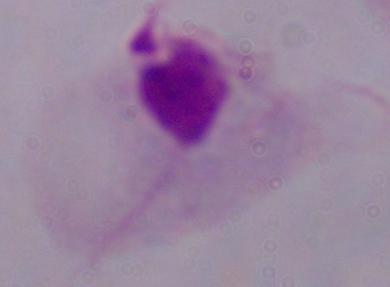

Summary:
  - Modality: photomicrograph
  - Identification: trichomonad
  - Magnification: 1000x